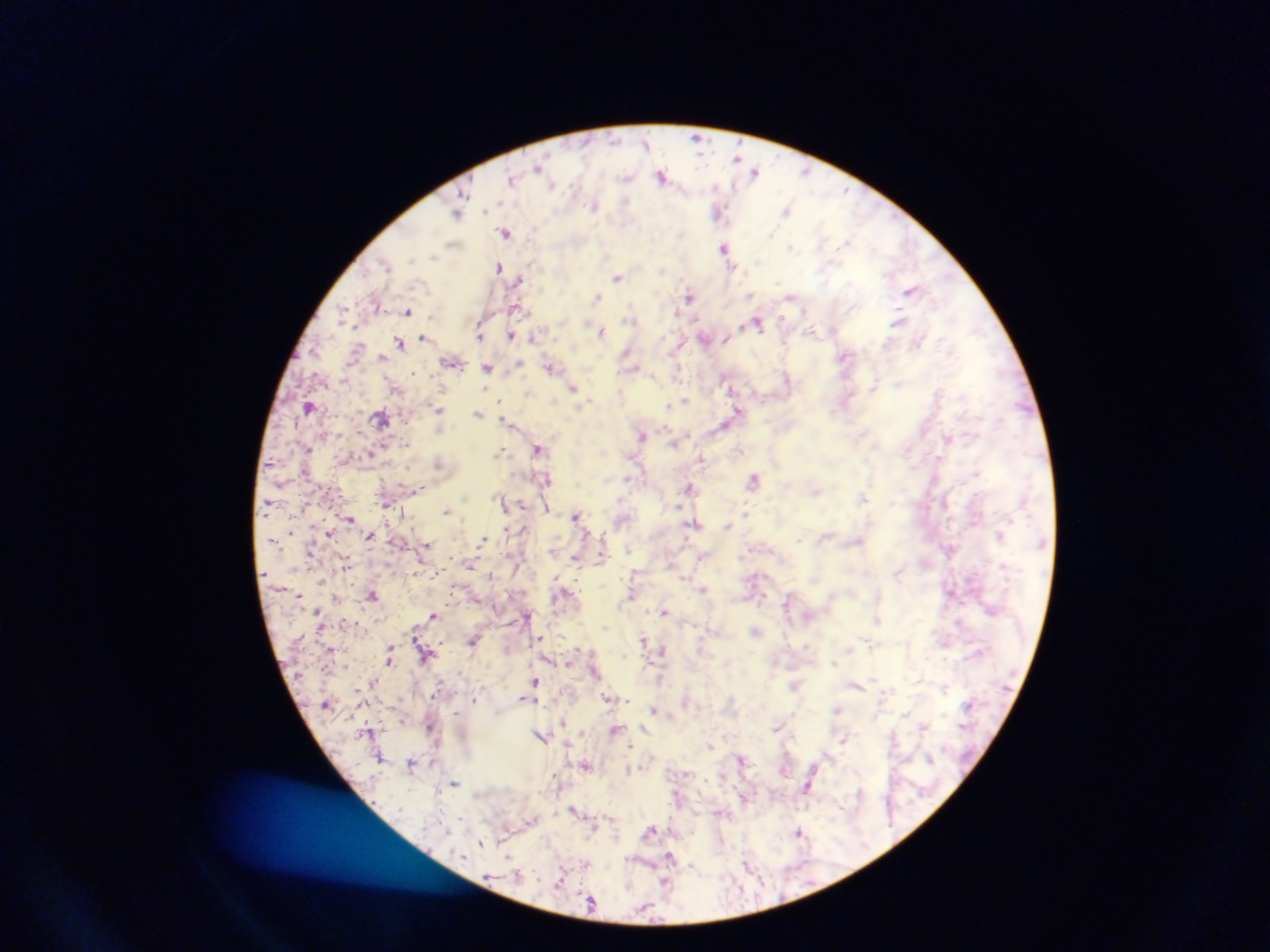

field of view = single
country = Ghana
preparation = thick blood smear
Plasmodium parasite locations = approximate centers as x y in pixels: 697 137; 646 144; 739 156; 539 168; 756 171; 806 171; 661 176; 514 178; 627 178; 552 184; 595 205; 719 210; 788 210; 457 213; 506 232; 727 249; 500 267; 618 277; 519 280; 912 289; 751 295; 690 296; 790 296; 598 298; 376 302; 518 307; 408 311; 900 320; 758 322; 600 331; 481 333; 512 334; 425 337; 534 337; 705 338; 400 342; 628 353; 845 356; 382 357; 452 362; 519 365; 551 366; 488 369; 899 384; 574 388; 686 400; 669 406; 309 407; 439 409; 739 411; 478 414; 382 417; 509 422; 726 423; 643 435; 948 439; 676 442; 538 448; 308 449; 502 450; 370 453; 703 459; 754 479; 545 481; 689 487; 815 491; 864 497; 504 502; 386 503; 547 507; 447 510; 577 516; 350 518; 696 524; 728 526; 508 529; 329 534; 370 535; 1000 535; 483 540; 427 545; 553 550; 576 556; 603 556; 672 564; 347 565; 898 573; 491 574; 703 588; 951 592; 299 594; 632 594; 373 595; 336 597; 787 603; 319 611; 664 611; 434 614; 528 614; 877 619; 756 630; 542 638; 645 639; 474 640; 869 642; 390 647; 579 648; 662 651; 426 652; 390 662; 568 662; 595 671; 662 678; 375 681; 535 681; 856 684; 795 685; 525 698; 609 698; 474 699; 535 700; 685 701; 654 708; 837 709; 402 720; 563 721; 431 725; 924 725; 778 726; 646 727; 617 729; 542 736; 844 738; 380 756; 743 758; 412 762; 586 765; 814 767; 454 783; 807 788; 574 809; 651 830; 799 831; 481 844; 671 857; 749 863; 561 881; 664 884; 591 900
capture = mobile-phone photograph through a microscope
image size = 1270×952 pixels